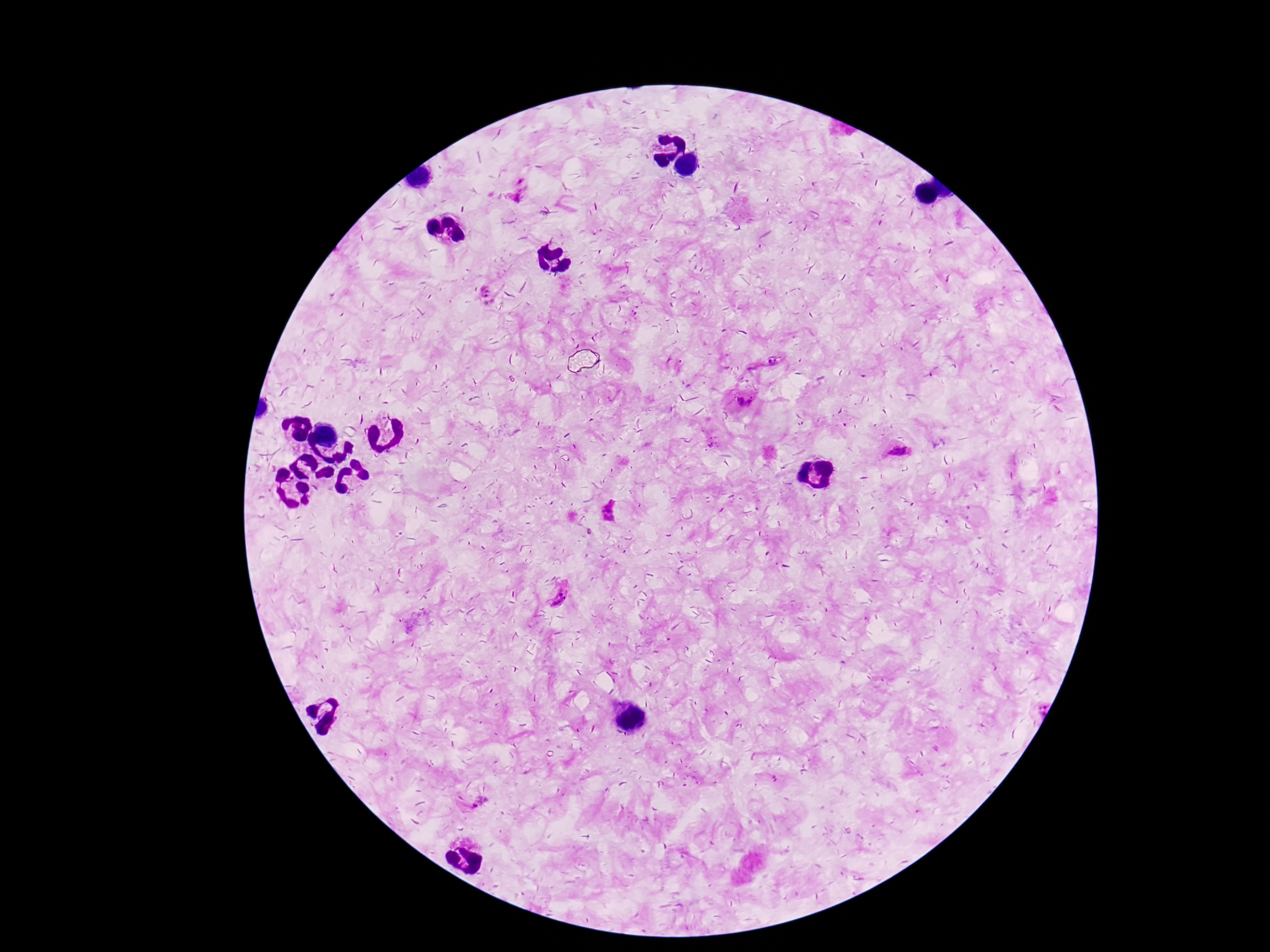
stain = Giemsa
preparation = thick blood film
Plasmodium parasite locations = approximate centers as (x, y) in pixels: (521, 188), (485, 290), (765, 363), (745, 401), (898, 454), (611, 510), (563, 597), (478, 801)
capture = smartphone camera through the microscope eyepiece
image size = 1270×952 pixels
magnification = 100x
patient malaria status = positive
field of view = single